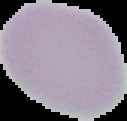

Summary:
  - Preparation: thin blood smear
  - Result: negative for Plasmodium parasites
  - Image type: cell region segmented out of the field of view; surrounding area masked to black
  - Image size: 127×121 pixels